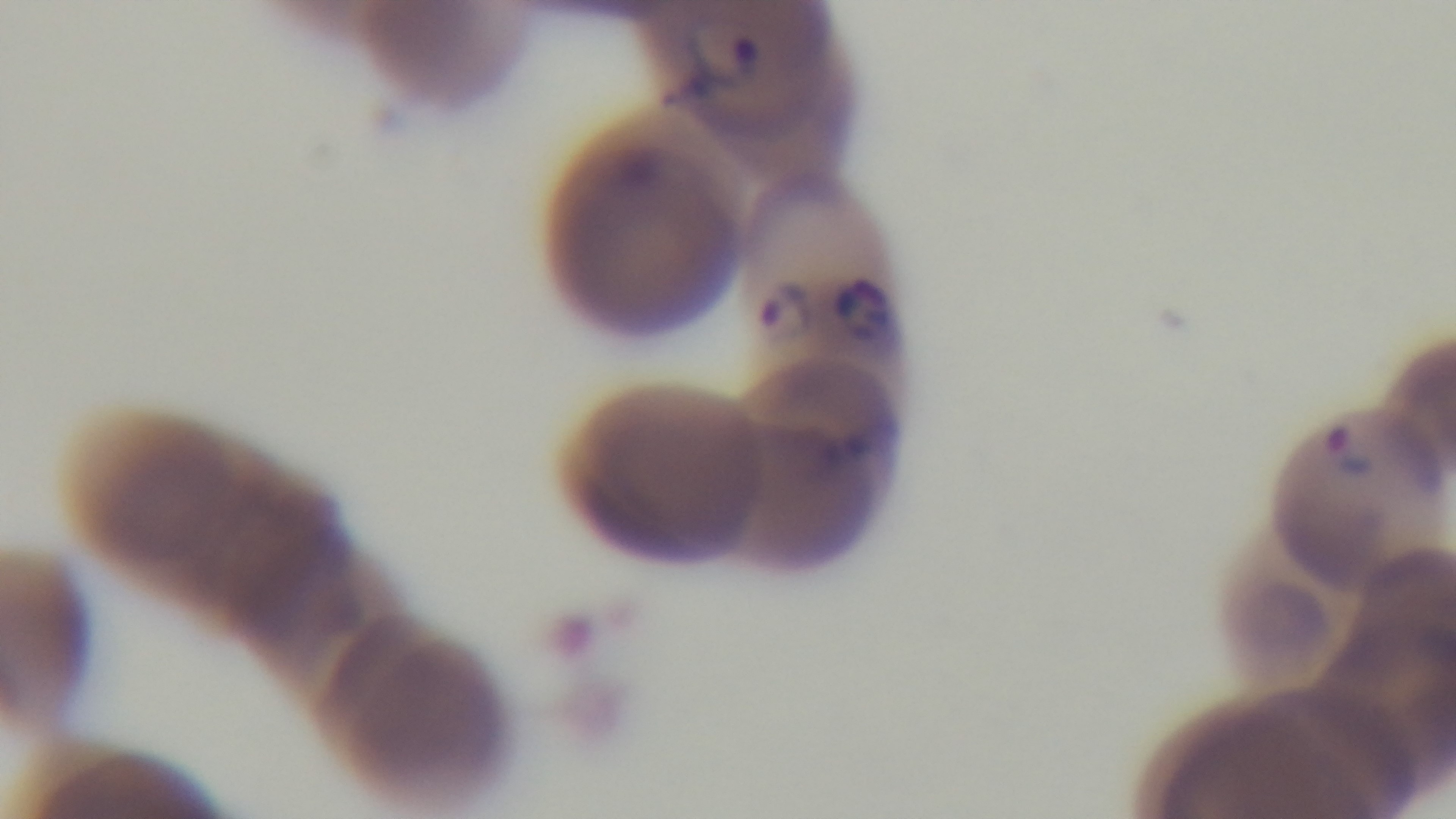
One field from the slide. Mounted 4K digital camera. Malaria status: positive. Oil-immersion objective, 100x. Preparation: thin. Giemsa stain. Light microscopy.